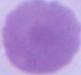

An erythrocyte is seen. Micrograph. 1000x magnification.